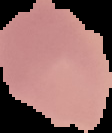 Segmented cell region on a black background. Malaria status: uninfected. From a thin blood smear. Image is 112×133 pixels.